Comment on the morphology of the erythrocytes.
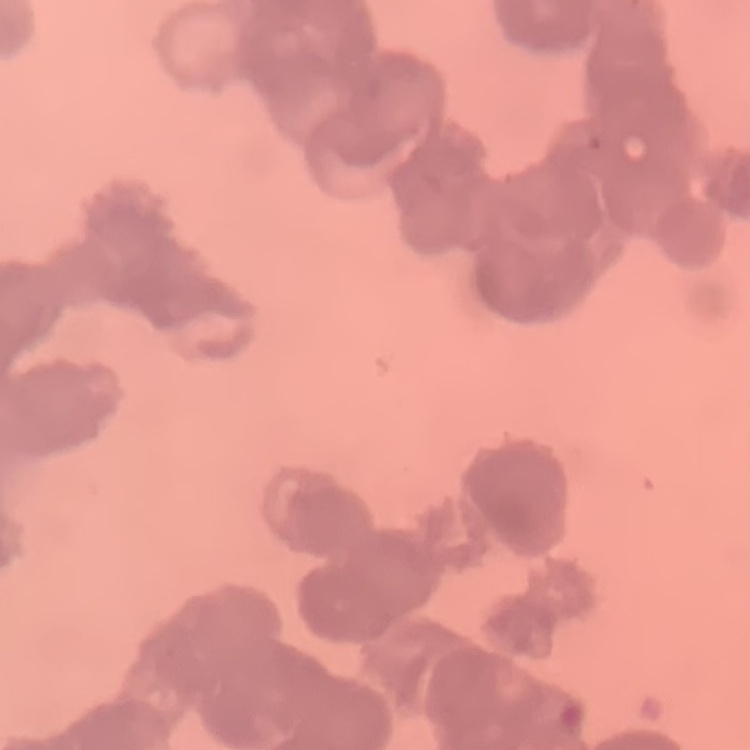

They show rouleaux formation.

Summary:
  - Preparation: thin blood smear
  - Stain: Field's or Giemsa
  - Image type: one tile cut from a larger photomicrograph